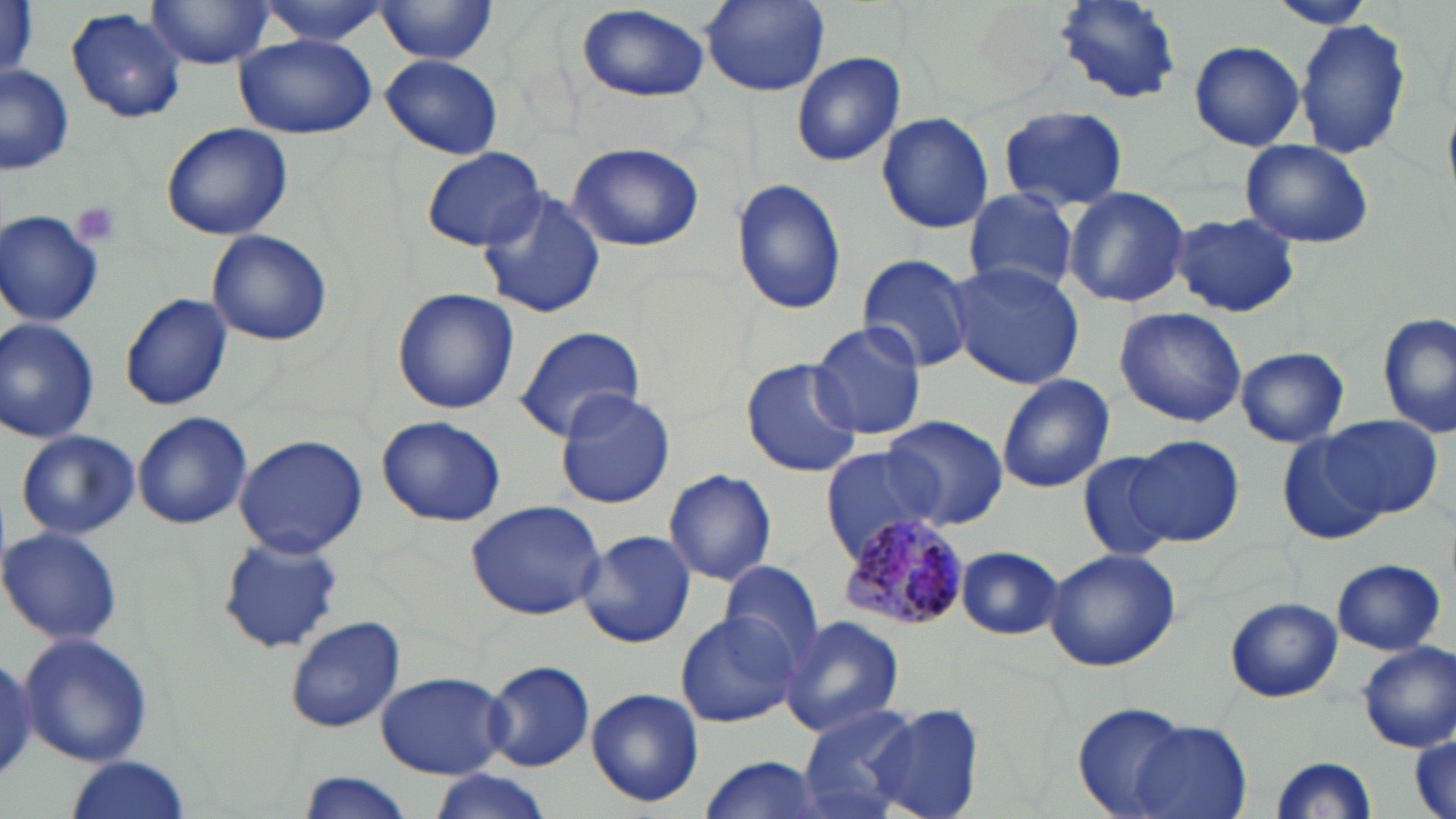
Summary:
  - Coordinate format: approximate bounding boxes as named x1/y1/x2/y2 corners in pixels
  - Uninfected red blood cell locations: (x1=0, y1=0, x2=38, y2=79), (x1=253, y1=0, x2=393, y2=43), (x1=374, y1=0, x2=498, y2=65), (x1=697, y1=0, x2=832, y2=98), (x1=1054, y1=0, x2=1183, y2=105), (x1=1269, y1=0, x2=1379, y2=31), (x1=146, y1=1, x2=276, y2=69), (x1=575, y1=5, x2=714, y2=104), (x1=66, y1=7, x2=189, y2=124), (x1=1294, y1=16, x2=1411, y2=162), (x1=233, y1=34, x2=375, y2=140), (x1=1187, y1=40, x2=1306, y2=152), (x1=791, y1=52, x2=906, y2=166), (x1=381, y1=54, x2=503, y2=160), (x1=0, y1=65, x2=75, y2=177), (x1=998, y1=105, x2=1129, y2=211), (x1=876, y1=111, x2=992, y2=234), (x1=161, y1=122, x2=293, y2=241), (x1=1239, y1=139, x2=1374, y2=249), (x1=566, y1=141, x2=705, y2=252), (x1=422, y1=148, x2=547, y2=253), (x1=731, y1=177, x2=845, y2=317), (x1=473, y1=185, x2=606, y2=319), (x1=1063, y1=185, x2=1190, y2=308), (x1=961, y1=188, x2=1082, y2=296), (x1=0, y1=209, x2=105, y2=328), (x1=1167, y1=213, x2=1304, y2=317), (x1=205, y1=230, x2=333, y2=347), (x1=857, y1=253, x2=976, y2=374), (x1=946, y1=262, x2=1086, y2=389), (x1=391, y1=287, x2=520, y2=415), (x1=120, y1=293, x2=234, y2=411), (x1=1113, y1=305, x2=1246, y2=427), (x1=1378, y1=315, x2=1455, y2=439), (x1=809, y1=318, x2=927, y2=440), (x1=0, y1=319, x2=100, y2=444), (x1=511, y1=323, x2=647, y2=444), (x1=1235, y1=347, x2=1350, y2=448), (x1=738, y1=357, x2=862, y2=477), (x1=996, y1=373, x2=1115, y2=493), (x1=555, y1=388, x2=677, y2=509), (x1=132, y1=411, x2=254, y2=531), (x1=883, y1=413, x2=1010, y2=529), (x1=1326, y1=413, x2=1443, y2=519), (x1=376, y1=415, x2=507, y2=528), (x1=16, y1=429, x2=140, y2=539), (x1=1280, y1=431, x2=1389, y2=547), (x1=233, y1=433, x2=368, y2=557), (x1=1128, y1=435, x2=1244, y2=546), (x1=819, y1=446, x2=944, y2=558), (x1=1078, y1=451, x2=1178, y2=562), (x1=662, y1=468, x2=777, y2=586), (x1=465, y1=498, x2=609, y2=621), (x1=1, y1=525, x2=124, y2=645), (x1=578, y1=530, x2=696, y2=649), (x1=218, y1=535, x2=344, y2=654), (x1=955, y1=546, x2=1063, y2=639), (x1=1044, y1=548, x2=1181, y2=673), (x1=719, y1=559, x2=826, y2=670), (x1=1331, y1=559, x2=1446, y2=654), (x1=1225, y1=597, x2=1342, y2=703), (x1=675, y1=611, x2=800, y2=729), (x1=283, y1=614, x2=403, y2=733), (x1=780, y1=616, x2=905, y2=736), (x1=19, y1=632, x2=154, y2=765), (x1=1357, y1=642, x2=1456, y2=752), (x1=0, y1=653, x2=35, y2=787), (x1=482, y1=659, x2=594, y2=773), (x1=376, y1=671, x2=507, y2=779), (x1=585, y1=687, x2=703, y2=809), (x1=1071, y1=702, x2=1193, y2=819), (x1=865, y1=704, x2=985, y2=819), (x1=797, y1=705, x2=921, y2=819), (x1=1130, y1=721, x2=1253, y2=819), (x1=1412, y1=733, x2=1454, y2=819), (x1=694, y1=754, x2=825, y2=819), (x1=1267, y1=755, x2=1377, y2=817), (x1=61, y1=757, x2=194, y2=819), (x1=423, y1=769, x2=553, y2=818), (x1=295, y1=773, x2=418, y2=819)
  - Plasmodium malariae-infected red blood cell locations: (x1=834, y1=511, x2=974, y2=634)
  - Platelet locations: (x1=68, y1=199, x2=125, y2=251)
  - Slide-level diagnosis: Plasmodium malariae
  - Preparation: thin blood smear
  - Image size: 1456×819 pixels
  - Modality: optical microscopy
  - Magnification: 1000x
  - Field of view: one of a larger specimen
  - Stain: May-Grünwald-Giemsa